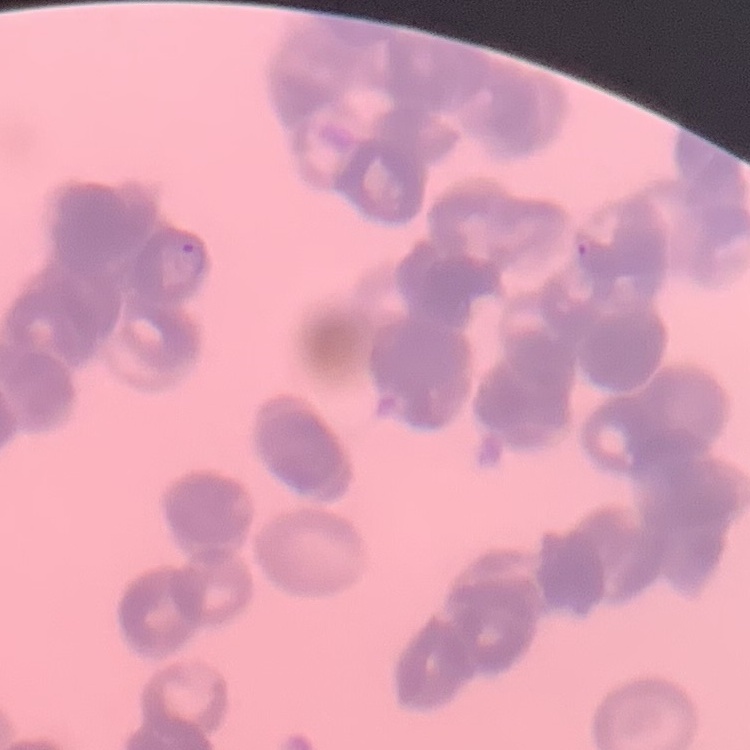

Summary:
  - Red blood cell morphology: rouleaux formation
  - Image type: one tile cut from a larger photomicrograph
  - Preparation: thin blood film
  - Stain: Field's or Giemsa